Classify this cell by malaria status.
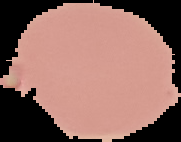

Uninfected.

Summary:
  - Image size: 181×142 pixels
  - Preparation: thin blood film
  - Image type: cell region segmented out of the field of view; surrounding area masked to black